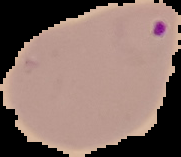

Summary:
  - Image type: cell region segmented out of the field of view; surrounding area masked to black
  - Result: malaria parasites detected
  - Image size: 181×157 pixels
  - Preparation: thin blood smear